Assess for Plasmodium parasites.
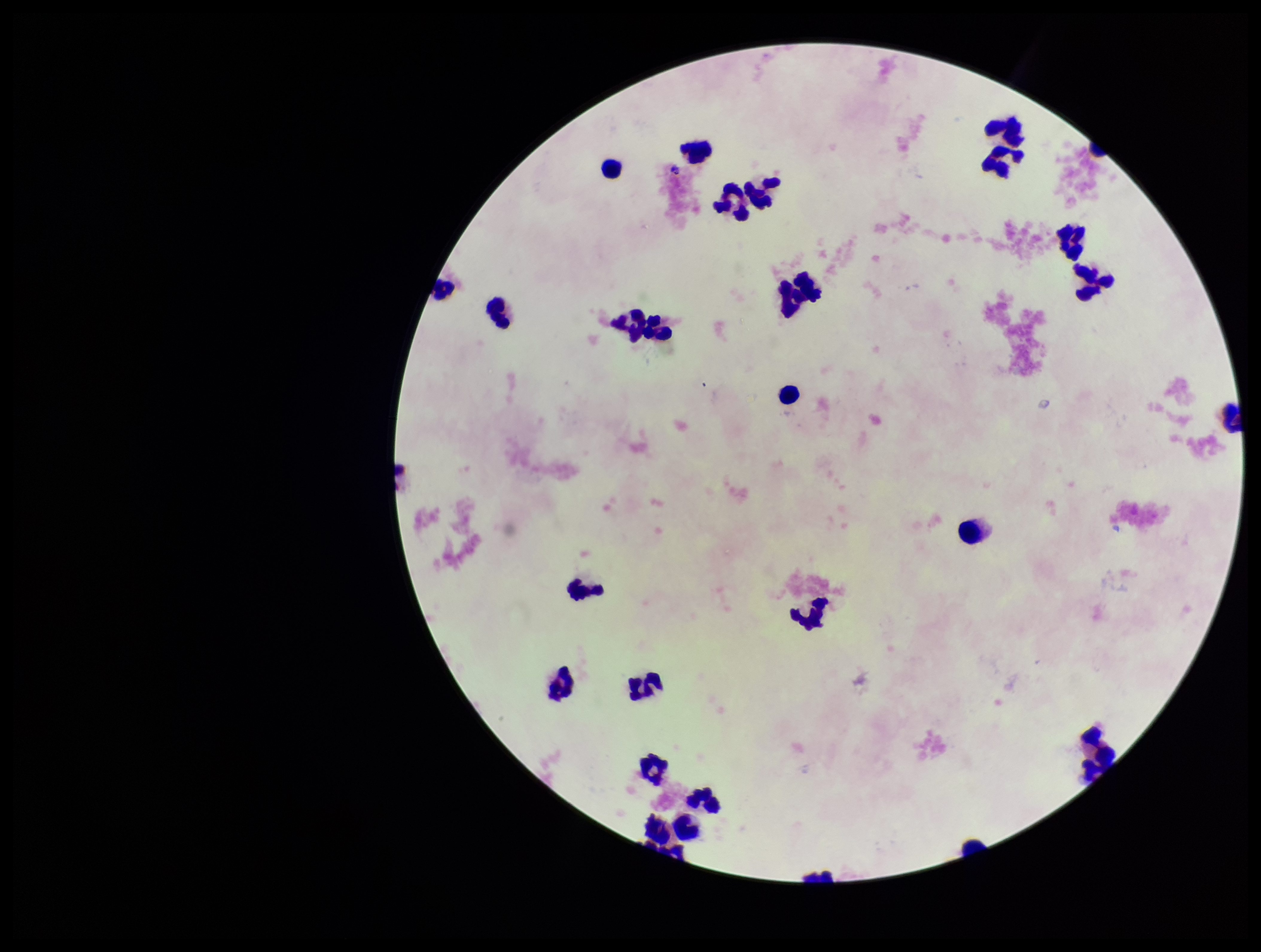

None seen.

Summary:
  - Parasite count: 0
  - Capture: smartphone photograph through the microscope eyepiece
  - Preparation: thick blood smear
  - Patient malaria status: negative
  - Field of view: one from this slide
  - Image size: 1261×952 pixels
  - Leukocyte count: 28
  - Stain: Giemsa